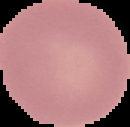

Summary:
  - Preparation: thin blood film
  - Image size: 130×127 pixels
  - Malaria status: uninfected
  - Image type: segmented cell region with the area outside set to black